Classify this cell by malaria status.
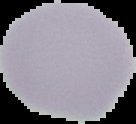

Uninfected.

Summary:
  - Image size: 136×124 pixels
  - Preparation: thin blood film
  - Image type: segmented cell region on a black background